Name the parasite shown.
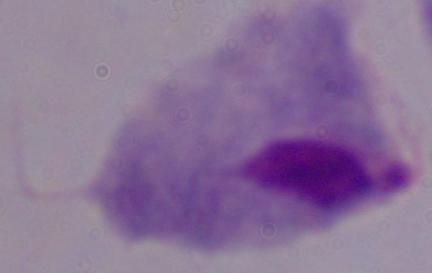
This is a trichomonad.

{
  "magnification": "1000x",
  "modality": "micrograph"
}